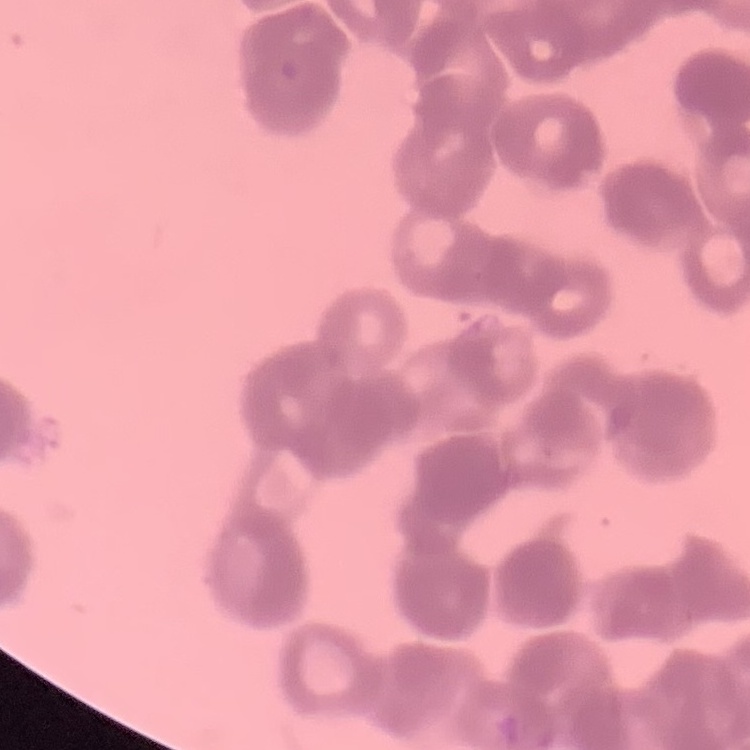
red blood cell morphology = rouleaux formation
image type = square crop of a larger photomicrograph
preparation = thin peripheral smear
stain = Field's or Giemsa